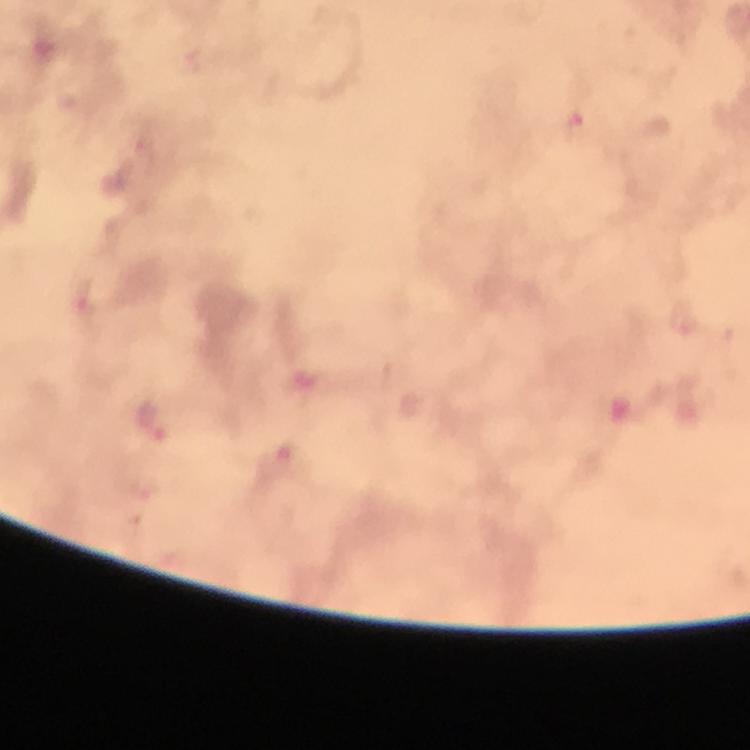

{
  "cropped_from": "a single field of view",
  "magnification": "100x",
  "preparation": "thick blood smear",
  "malaria_parasite_locations": "approximate centers as (x, y) in pixels: (576, 126), (83, 301), (684, 319), (156, 422), (281, 461)",
  "capture": "smartphone camera through the microscope",
  "image_size": "750×750 pixels",
  "context": "from a diagnostic examination for malaria",
  "stain": "Giemsa",
  "immersion_oil": "used"
}